Give the preparation type.
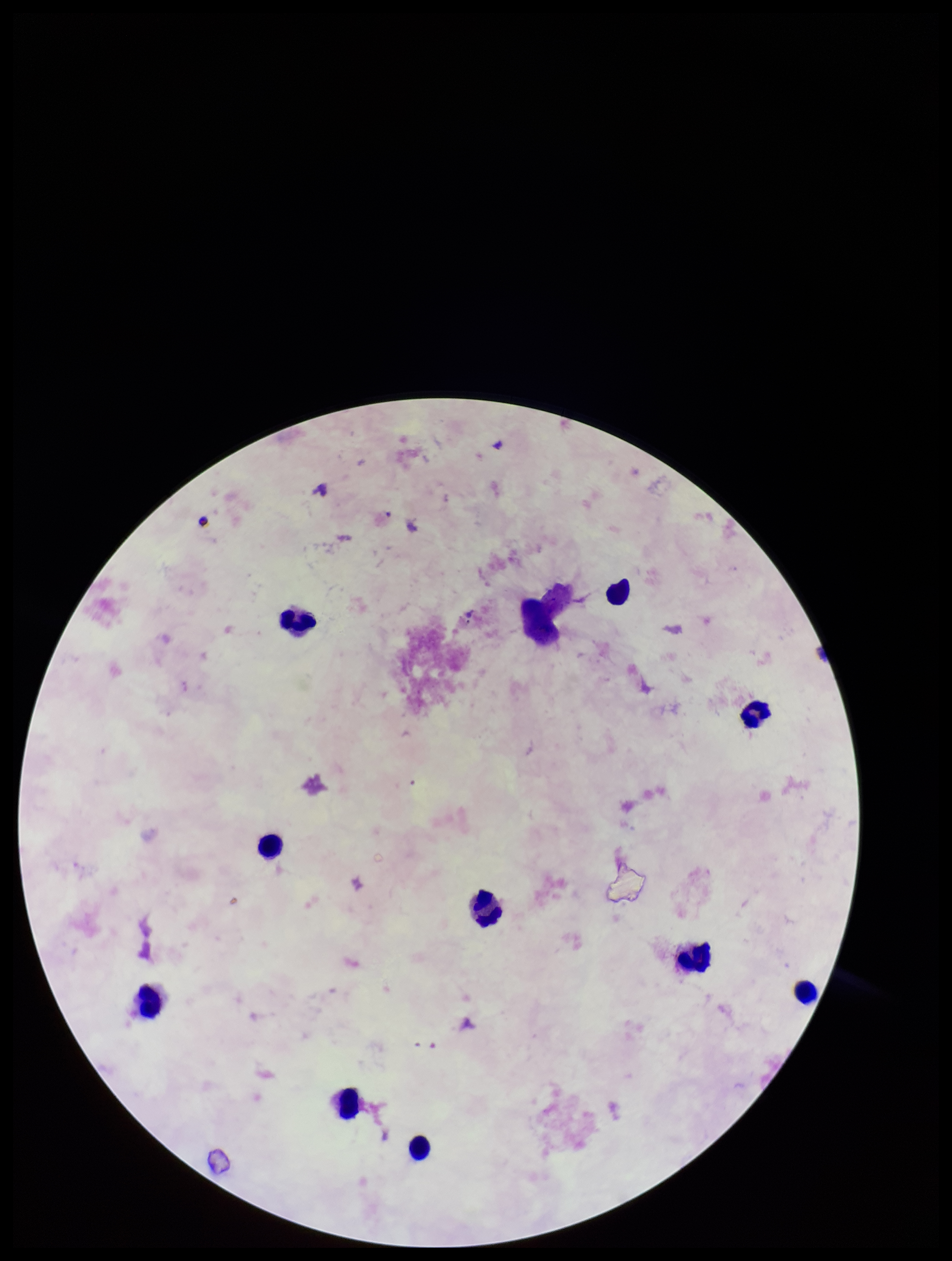
It is a thick blood smear.

Summary:
  - Stain: Giemsa
  - Capture: smartphone photograph through the microscope eyepiece
  - Field of view: single
  - Patient malaria status: negative
  - Leukocyte count: 10
  - Parasite count: 0
  - Plasmodium parasites: none seen
  - Image size: 952×1261 pixels